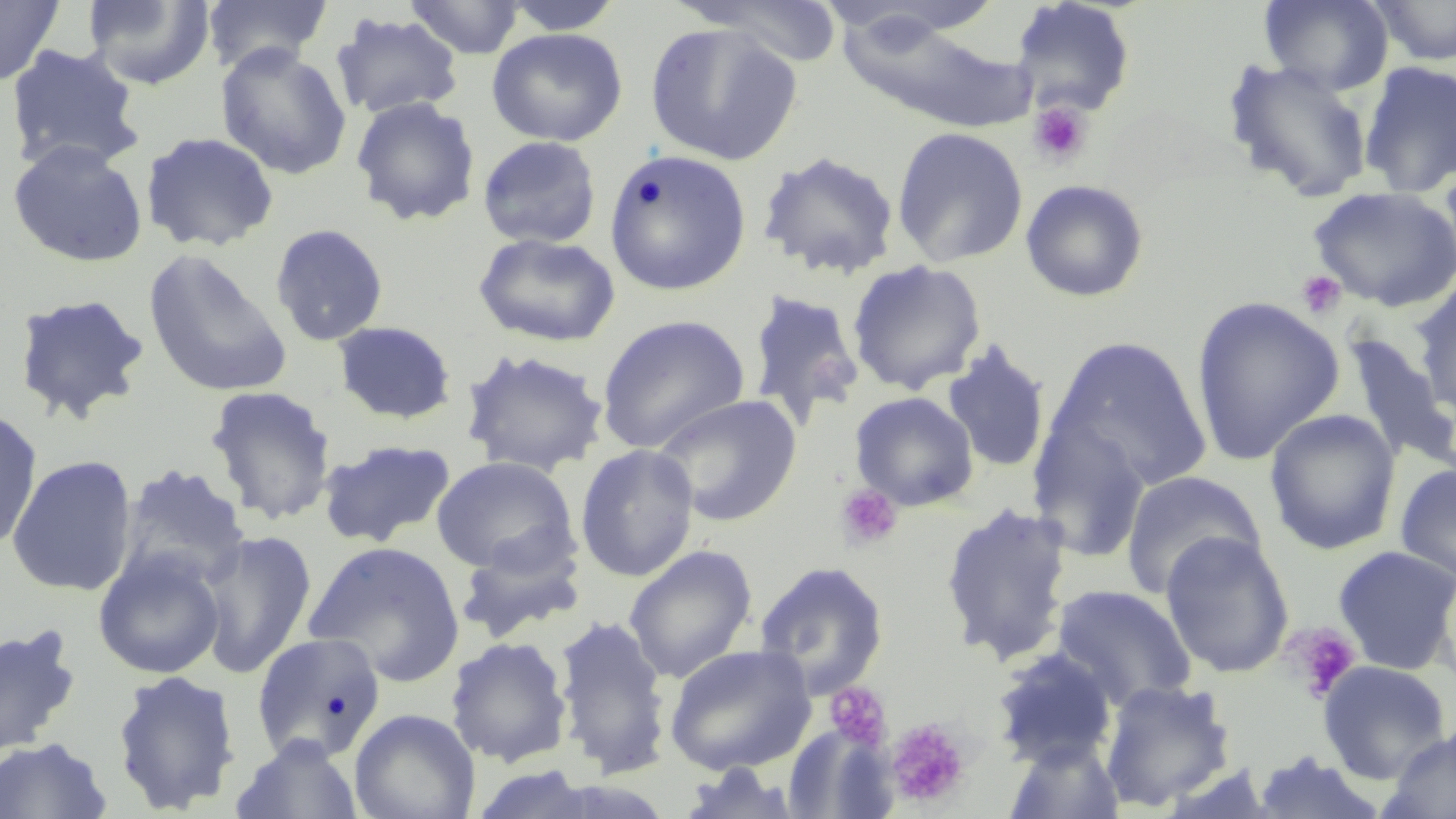 Approximate bounding boxes as named x1/y1/x2/y2 corners in pixels. Platelet locations: (x1=1027, y1=101, x2=1093, y2=167), (x1=1296, y1=270, x2=1346, y2=319), (x1=835, y1=483, x2=903, y2=552), (x1=1284, y1=622, x2=1362, y2=702), (x1=824, y1=682, x2=893, y2=752), (x1=886, y1=718, x2=969, y2=809). Uninfected red blood cell locations: (x1=0, y1=0, x2=66, y2=88), (x1=82, y1=0, x2=216, y2=90), (x1=201, y1=0, x2=332, y2=74), (x1=404, y1=0, x2=526, y2=58), (x1=498, y1=0, x2=627, y2=36), (x1=673, y1=0, x2=848, y2=66), (x1=1259, y1=0, x2=1395, y2=94), (x1=1369, y1=0, x2=1456, y2=66), (x1=1009, y1=1, x2=1137, y2=115), (x1=329, y1=12, x2=465, y2=120), (x1=830, y1=12, x2=1051, y2=128), (x1=645, y1=22, x2=803, y2=166), (x1=486, y1=28, x2=628, y2=146), (x1=4, y1=42, x2=146, y2=173), (x1=215, y1=43, x2=352, y2=180), (x1=1222, y1=59, x2=1375, y2=203), (x1=1358, y1=60, x2=1456, y2=198), (x1=350, y1=96, x2=481, y2=227), (x1=891, y1=126, x2=1029, y2=268), (x1=140, y1=131, x2=280, y2=253), (x1=477, y1=135, x2=602, y2=249), (x1=7, y1=139, x2=148, y2=268), (x1=604, y1=149, x2=751, y2=297), (x1=757, y1=150, x2=901, y2=279), (x1=1437, y1=161, x2=1456, y2=285), (x1=1019, y1=179, x2=1150, y2=302), (x1=1308, y1=186, x2=1456, y2=312), (x1=269, y1=222, x2=389, y2=347), (x1=473, y1=231, x2=621, y2=346), (x1=143, y1=250, x2=292, y2=398), (x1=846, y1=259, x2=987, y2=395), (x1=1411, y1=282, x2=1456, y2=423), (x1=745, y1=289, x2=866, y2=426), (x1=12, y1=292, x2=150, y2=423), (x1=1190, y1=295, x2=1344, y2=466), (x1=596, y1=314, x2=751, y2=455), (x1=331, y1=321, x2=456, y2=423), (x1=1342, y1=332, x2=1456, y2=471), (x1=1045, y1=336, x2=1213, y2=494), (x1=941, y1=341, x2=1052, y2=474), (x1=460, y1=348, x2=609, y2=476), (x1=204, y1=385, x2=337, y2=525), (x1=849, y1=390, x2=979, y2=511), (x1=652, y1=393, x2=802, y2=526), (x1=1263, y1=408, x2=1401, y2=555), (x1=0, y1=409, x2=43, y2=551), (x1=1026, y1=413, x2=1153, y2=562), (x1=317, y1=438, x2=457, y2=548), (x1=575, y1=444, x2=700, y2=583), (x1=6, y1=454, x2=138, y2=597), (x1=431, y1=456, x2=579, y2=574), (x1=119, y1=463, x2=252, y2=586), (x1=1395, y1=463, x2=1456, y2=590), (x1=1119, y1=469, x2=1266, y2=597), (x1=939, y1=502, x2=1075, y2=665), (x1=195, y1=529, x2=317, y2=679), (x1=1160, y1=531, x2=1295, y2=679), (x1=455, y1=535, x2=587, y2=644), (x1=303, y1=540, x2=466, y2=687), (x1=623, y1=544, x2=758, y2=684), (x1=1332, y1=545, x2=1456, y2=675), (x1=93, y1=550, x2=226, y2=679), (x1=752, y1=559, x2=890, y2=699), (x1=1049, y1=585, x2=1197, y2=710), (x1=549, y1=614, x2=676, y2=780), (x1=0, y1=622, x2=83, y2=755), (x1=249, y1=632, x2=386, y2=764), (x1=444, y1=636, x2=574, y2=767), (x1=663, y1=644, x2=817, y2=776), (x1=989, y1=648, x2=1120, y2=767), (x1=1316, y1=660, x2=1452, y2=784), (x1=110, y1=668, x2=244, y2=815), (x1=1099, y1=679, x2=1236, y2=812), (x1=349, y1=708, x2=481, y2=819), (x1=783, y1=724, x2=898, y2=819), (x1=1381, y1=728, x2=1456, y2=819), (x1=231, y1=736, x2=362, y2=819), (x1=0, y1=737, x2=113, y2=819), (x1=1002, y1=737, x2=1126, y2=819), (x1=1248, y1=752, x2=1388, y2=819). Slide-level diagnosis: negative for blood parasites. 1000x magnification. Optical microscopy. Image is 1456×819 pixels. Thin blood film. May-Grünwald-Giemsa-stained preparation. Single field of view.